Assess this cell for malaria.
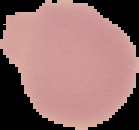

It is uninfected.

From a thin blood smear. Image is 139×130 pixels. Segmented cell region on a black background.